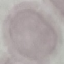 Result: no malaria parasites detected. Giemsa-stained preparation. Thin blood film. Cell patch, automatically extracted from a larger field of view and resized to 64 × 64 pixels. Photographed with a smartphone camera at the microscope eyepiece.